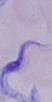
Summary:
  - Modality: photomicrograph
  - Magnification: 1000x
  - Identification: trypanosome